Comment on the morphology of the erythrocytes.
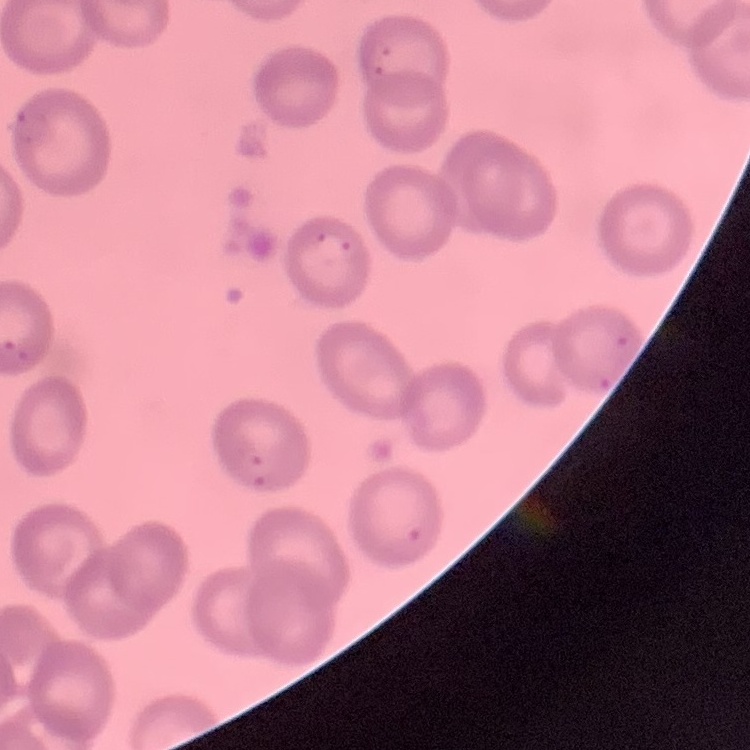

No rouleaux formation.

{
  "image_type": "square crop of a larger photomicrograph",
  "preparation": "thin peripheral smear",
  "stain": "Field's or Giemsa"
}